Name the cell type shown.
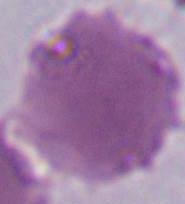

This is an erythrocyte.

Summary:
  - Magnification: 1000x
  - Modality: photomicrograph